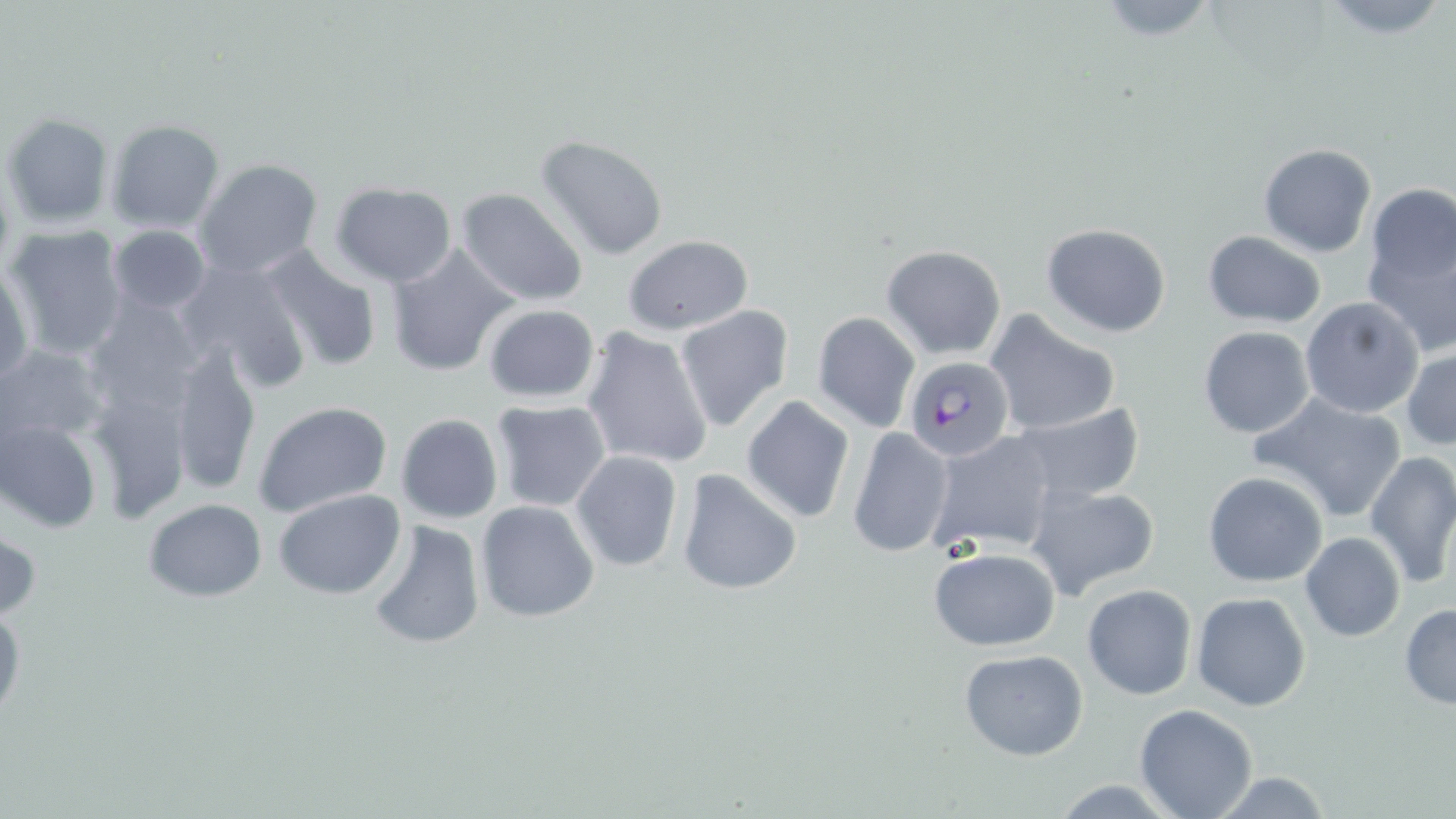

Summary:
  - Coordinate format: approximate bounding boxes as [x1, y1, x2, y2] in pixels
  - Uninfected red blood cell locations: [1090, 0, 1223, 43], [1316, 0, 1452, 40], [2, 111, 115, 229], [105, 119, 225, 233], [536, 135, 669, 260], [1258, 142, 1378, 258], [193, 159, 326, 280], [329, 181, 456, 286], [457, 188, 588, 309], [1358, 195, 1455, 358], [1041, 222, 1171, 337], [108, 224, 211, 315], [4, 225, 130, 361], [1201, 231, 1326, 327], [621, 235, 752, 335], [384, 243, 519, 378], [880, 245, 1008, 360], [255, 246, 383, 373], [1, 259, 35, 387], [177, 259, 309, 392], [80, 293, 207, 423], [1300, 296, 1425, 418], [482, 303, 600, 404], [673, 304, 795, 432], [982, 309, 1123, 438], [811, 311, 921, 432], [581, 326, 715, 471], [1198, 326, 1317, 439], [169, 342, 261, 496], [0, 343, 106, 453], [1403, 345, 1456, 450], [84, 383, 192, 521], [1249, 392, 1409, 524], [740, 396, 856, 523], [253, 399, 394, 515], [490, 399, 614, 514], [1012, 403, 1144, 502], [395, 414, 504, 524], [1, 418, 102, 533], [847, 427, 955, 559], [929, 431, 1059, 554], [570, 450, 684, 572], [1363, 450, 1456, 592], [676, 471, 802, 593], [1203, 471, 1330, 589], [1026, 482, 1161, 600], [274, 490, 403, 599], [142, 498, 267, 601], [474, 500, 599, 623], [366, 520, 487, 650], [0, 527, 40, 625], [1300, 532, 1405, 642], [927, 545, 1061, 651], [1082, 585, 1197, 699], [1192, 592, 1310, 711], [0, 602, 25, 725], [1399, 602, 1456, 708], [958, 648, 1089, 761], [1133, 704, 1259, 819], [1201, 769, 1339, 818], [1046, 779, 1185, 817]
  - Plasmodium falciparum-infected red blood cell locations: [904, 355, 1014, 461]
  - Slide-level diagnosis: Plasmodium falciparum
  - Preparation: thin blood smear
  - Image size: 1456×819 pixels
  - Field of view: single
  - Modality: optical microscopy
  - Magnification: 1000x
  - Stain: May-Grünwald-Giemsa